Give the position of every Plasmodium parasite.
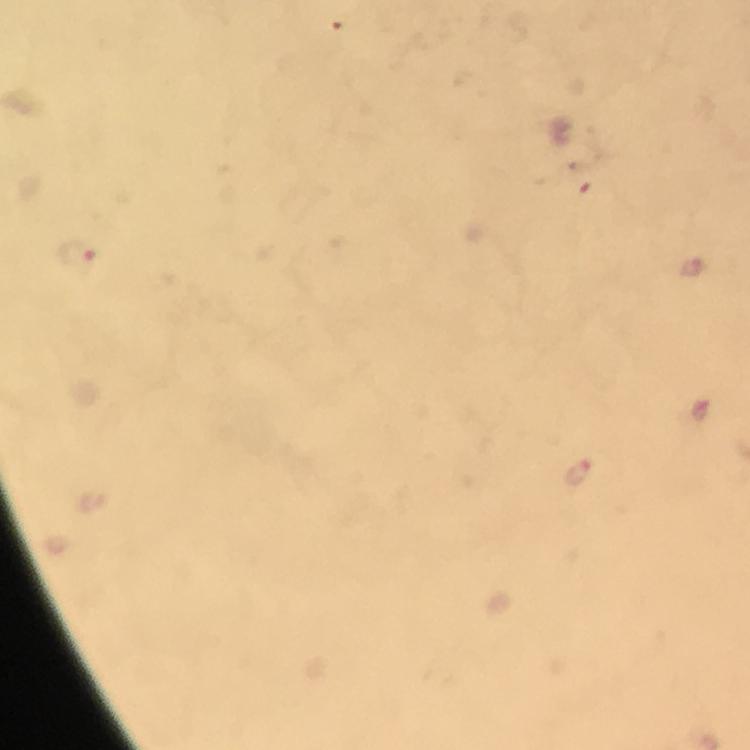

Approximate centers as {x, y} in pixels.
Plasmodium parasites: {77, 257}, {577, 470}.

context: from a diagnostic examination for malaria
preparation: thick blood film
immersion_oil: applied
image_size: 750×750 pixels
stain: Giemsa
cropped_from: one field of view
capture: smartphone camera through the microscope
magnification: 100x